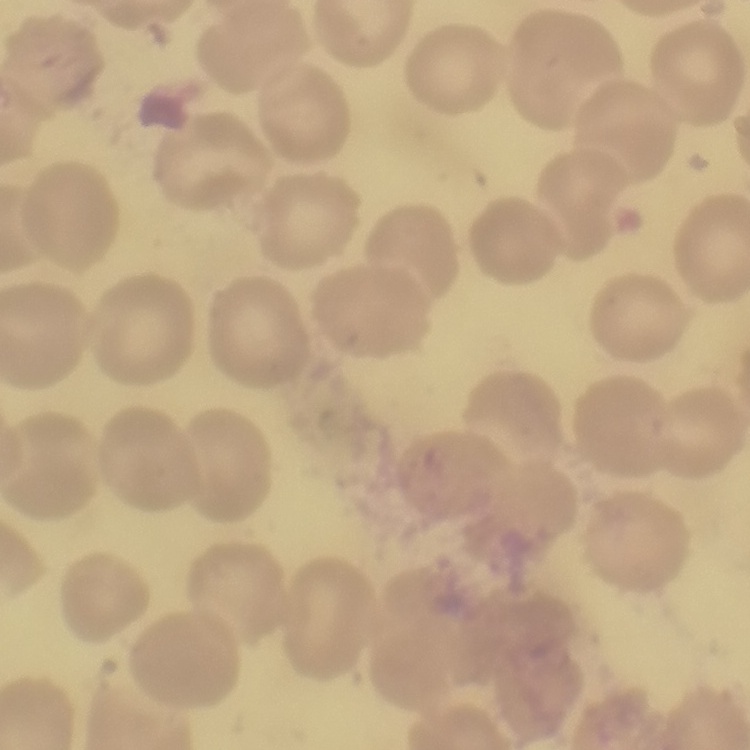
Summary:
  - Erythrocyte morphology: no rouleaux formation
  - Image type: one tile cut from a larger photomicrograph
  - Preparation: thin blood film
  - Stain: Field's or Giemsa